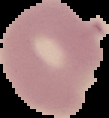 From a thin blood smear. Result: no malaria parasites detected. Segmented cell region on a black background. Image is 109×118 pixels.